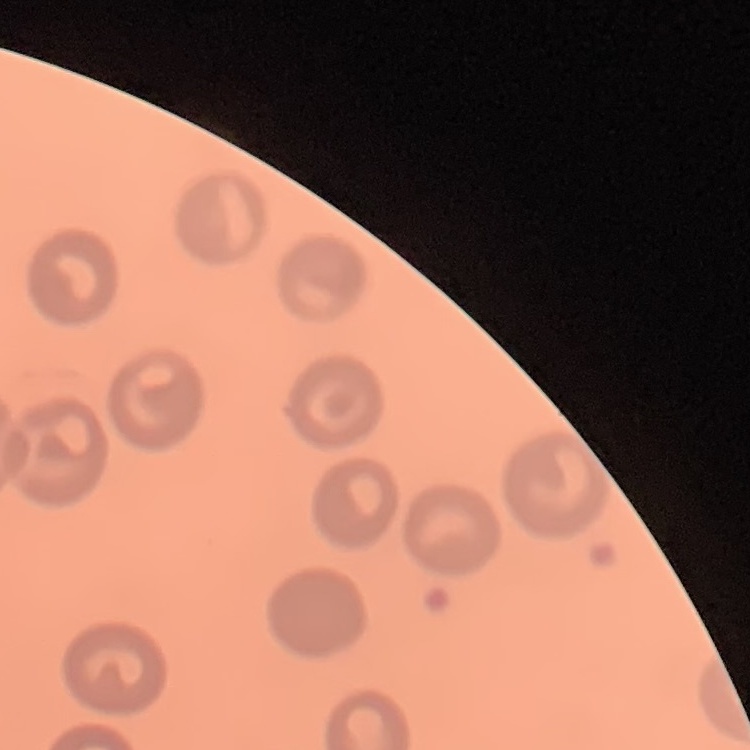
Summary:
  - Red blood cell morphology: no rouleaux formation
  - Image type: square crop of a larger photomicrograph
  - Stain: Field's or Giemsa
  - Preparation: thin peripheral smear